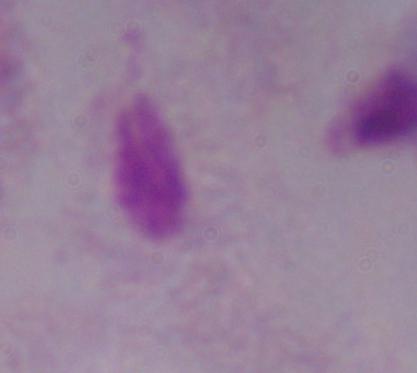

identification = trichomonad
modality = micrograph
magnification = 1000x